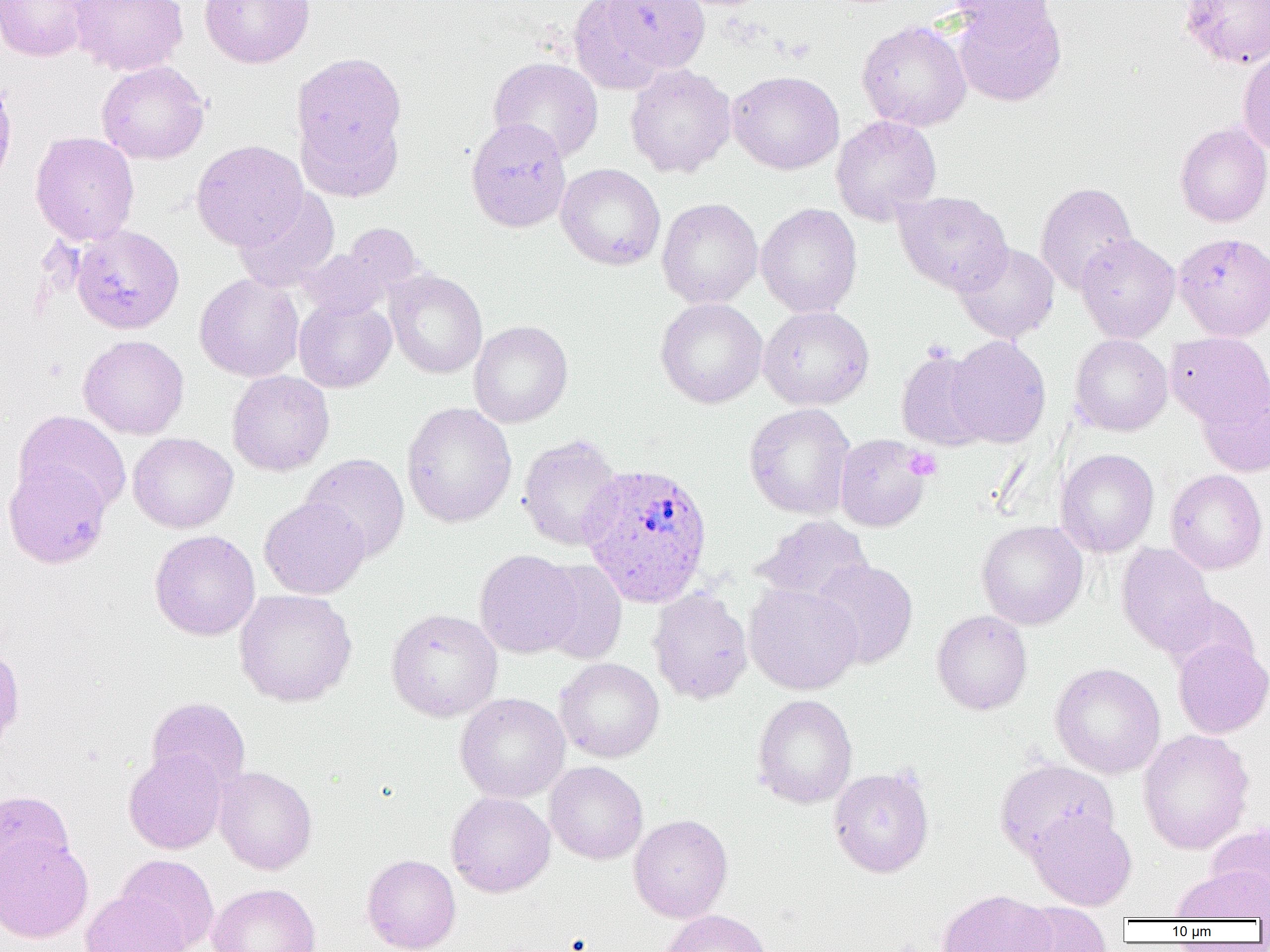

slide-level diagnosis = Plasmodium ovale
image size = 1270×952 pixels
modality = optical microscopy
magnification = 1000x
preparation = thin blood smear
platelet locations = approximate bounding boxes as (x1, y1, x2, y2) in pixels: (903, 448, 942, 481)
uninfected red blood cell locations = approximate bounding boxes as (x1, y1, x2, y2) in pixels: (0, 0, 91, 62), (69, 0, 188, 77), (199, 0, 315, 68), (599, 0, 709, 75), (946, 0, 1060, 43), (1179, 0, 1270, 68), (950, 1, 1067, 106), (857, 20, 972, 131), (291, 52, 407, 176), (1238, 52, 1270, 156), (488, 56, 603, 162), (97, 61, 210, 164), (624, 64, 736, 179), (727, 70, 844, 174), (0, 74, 17, 191), (296, 108, 404, 202), (831, 115, 942, 225), (465, 118, 572, 233), (1175, 122, 1270, 227), (29, 131, 140, 246), (191, 140, 308, 251), (556, 163, 665, 271), (1035, 182, 1138, 294), (233, 187, 340, 293), (893, 191, 1012, 294), (657, 198, 763, 309), (756, 203, 862, 318), (341, 223, 424, 299), (70, 224, 184, 335), (1075, 234, 1180, 343), (954, 242, 1060, 343), (297, 248, 390, 319), (385, 269, 487, 379), (194, 274, 304, 382), (294, 297, 396, 393), (655, 298, 767, 408), (758, 306, 874, 410), (468, 321, 573, 428), (1165, 332, 1270, 430), (1070, 334, 1172, 436), (78, 335, 189, 439), (946, 336, 1051, 448), (895, 348, 991, 451), (227, 371, 334, 476), (1196, 381, 1270, 477), (402, 402, 517, 528), (744, 403, 856, 520), (13, 410, 131, 517), (128, 432, 238, 533), (834, 433, 932, 532), (517, 434, 624, 552), (1056, 449, 1159, 557), (300, 453, 410, 563), (3, 461, 111, 568), (1165, 470, 1267, 574), (259, 497, 370, 600), (754, 516, 873, 604), (976, 520, 1088, 629), (149, 529, 260, 641), (1116, 543, 1218, 656), (474, 549, 583, 658), (535, 559, 627, 665), (811, 560, 918, 669), (743, 583, 863, 694), (648, 588, 753, 704), (233, 589, 358, 707), (1161, 593, 1259, 678), (386, 608, 503, 722), (932, 610, 1032, 715), (1172, 639, 1270, 738), (0, 644, 25, 754), (554, 658, 665, 763), (1050, 663, 1166, 778), (454, 692, 570, 803), (752, 694, 857, 808), (146, 697, 250, 793), (1137, 729, 1255, 855), (123, 750, 227, 854), (995, 758, 1118, 862), (545, 761, 648, 864), (214, 766, 317, 875), (828, 767, 934, 878), (0, 791, 75, 891), (446, 791, 555, 897), (1027, 809, 1137, 910), (628, 814, 732, 922), (1206, 823, 1270, 911), (0, 833, 93, 943), (115, 854, 219, 952), (362, 854, 461, 952), (1172, 866, 1270, 922), (207, 883, 321, 952), (937, 889, 1056, 952), (80, 890, 191, 952), (1008, 902, 1112, 952), (659, 909, 773, 952)
Plasmodium ovale-infected red blood cell locations = approximate bounding boxes as (x1, y1, x2, y2) in pixels: (579, 462, 714, 606)
field of view = one of a larger specimen